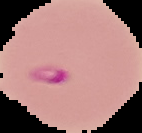
Malaria status: parasitized. From a thin blood film. Image is 142×133 pixels. Cell region segmented out of the field of view; the surrounding area is masked to black.